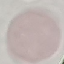

result: no malaria parasites detected
preparation: thin blood smear
image_type: cell patch, automatically extracted from a larger field of view and resized to 64 × 64 pixels
capture: smartphone through the microscope eyepiece
stain: Giemsa